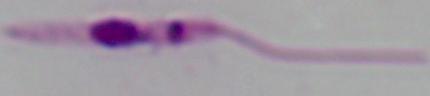

identification = Leishmania
modality = micrograph
magnification = 1000x